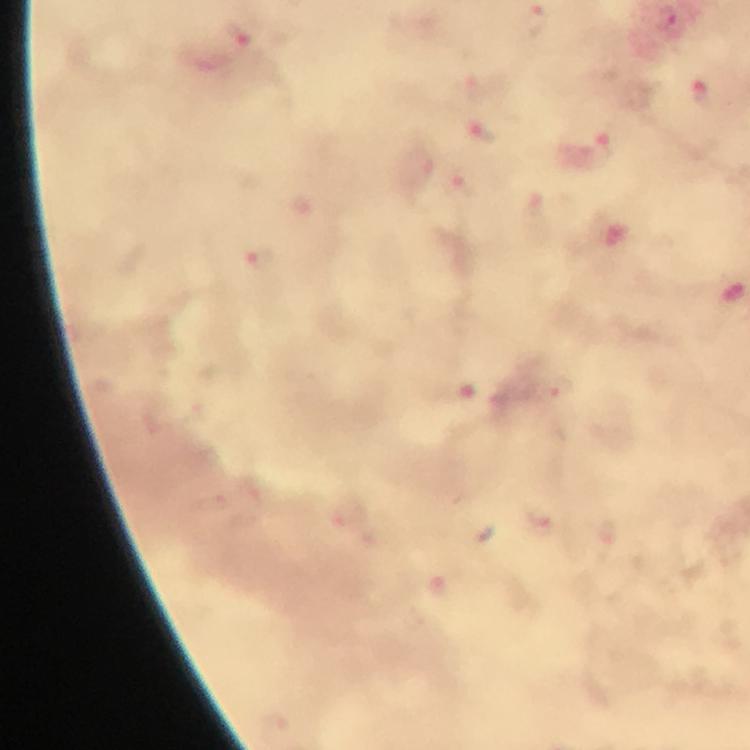
Approximate centers as (x, y) in pixels. Plasmodium parasite locations: (242, 36), (481, 132), (609, 157), (255, 256), (558, 390). Image is 750×750 pixels. Cropped region of a single field of view. Immersion oil was used. At 100x magnification. Giemsa stain. From a diagnostic examination for malaria. Thick smear. Smartphone photograph taken through a microscope.